Assess this cell for malaria.
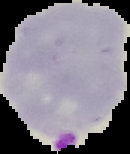
It is parasitized.

image type = cell region segmented out of the field of view; surrounding area masked to black
image size = 130×154 pixels
preparation = thin blood smear